Assess for parasitized red blood cells.
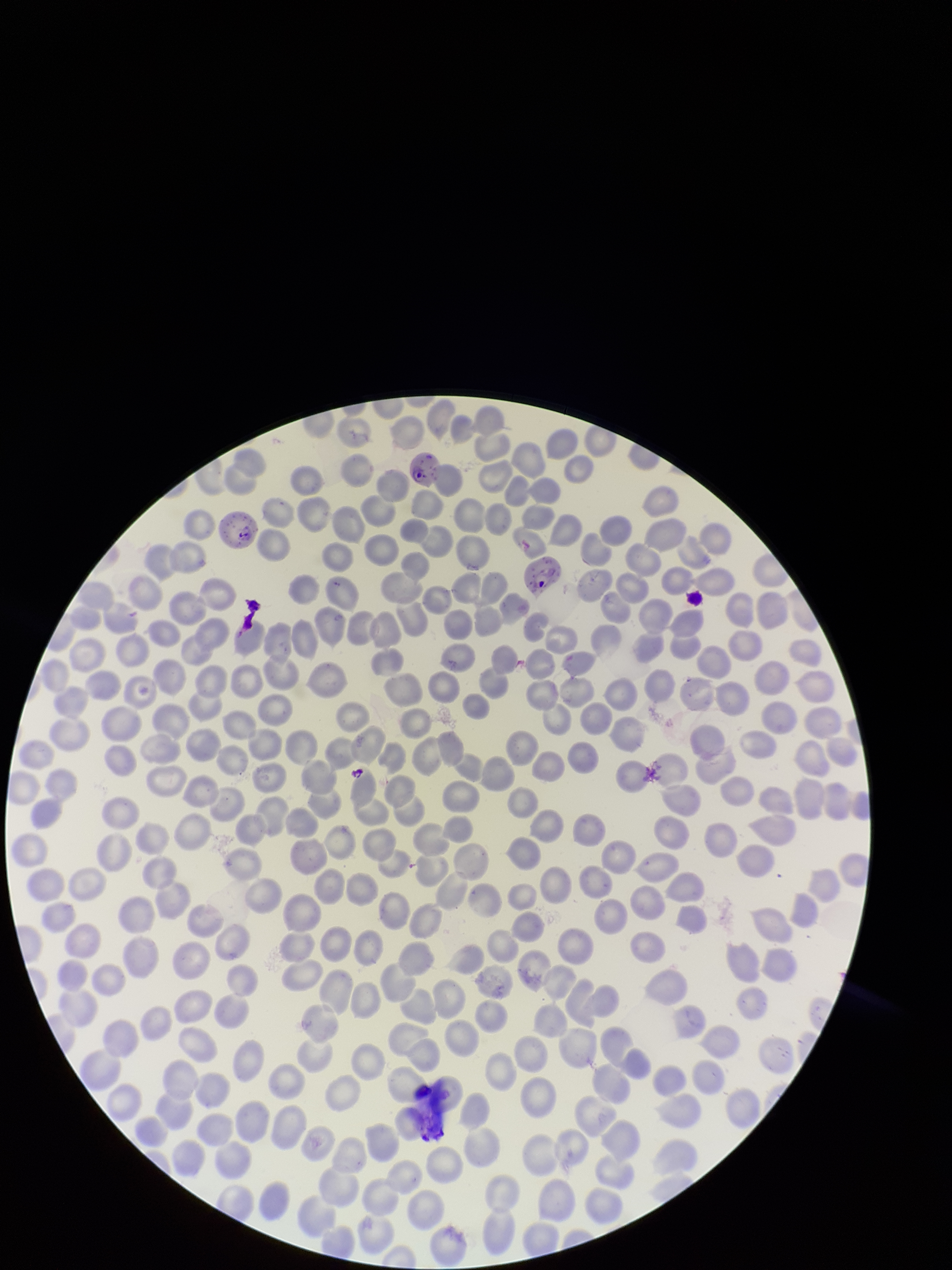
Seen.

Patient malaria status: infected. Single field of view. Preparation: thin. Giemsa stain. Smartphone photograph taken through the eyepiece of a microscope. Species reported for this patient: Plasmodium falciparum. Parasitized red blood cell count: 3. Red blood cell count: 300. Image is 952×1270 pixels.